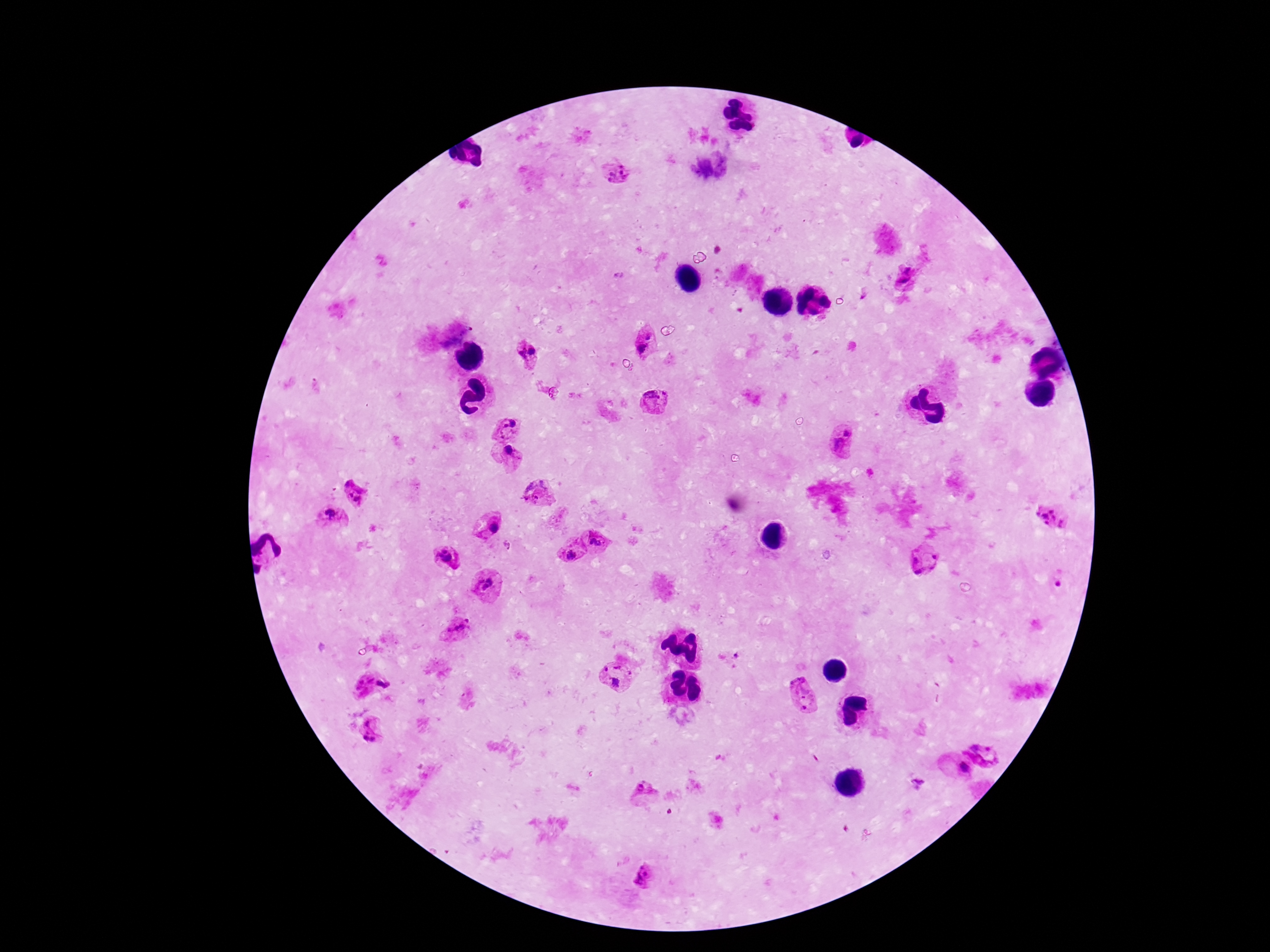

Approximate object centers, in pixels from the top-left corner.
Summary:
  - Plasmodium parasite locations: (x=619, y=173), (x=909, y=268), (x=903, y=282), (x=649, y=335), (x=642, y=348), (x=533, y=350), (x=521, y=354), (x=654, y=401), (x=508, y=423), (x=845, y=440), (x=509, y=454), (x=545, y=484), (x=529, y=485), (x=356, y=494), (x=533, y=500), (x=330, y=518), (x=1052, y=518), (x=495, y=528), (x=598, y=539), (x=569, y=550), (x=447, y=558), (x=924, y=559), (x=487, y=584), (x=460, y=626), (x=730, y=659), (x=618, y=676), (x=375, y=685), (x=806, y=694), (x=372, y=729), (x=987, y=746), (x=957, y=769), (x=646, y=792), (x=647, y=874)
  - Magnification: 100x
  - Patient malaria status: positive
  - Image size: 1270×952 pixels
  - Capture: smartphone camera through the microscope eyepiece
  - Stain: Giemsa
  - Field of view: one from this slide
  - Preparation: thick peripheral-blood smear